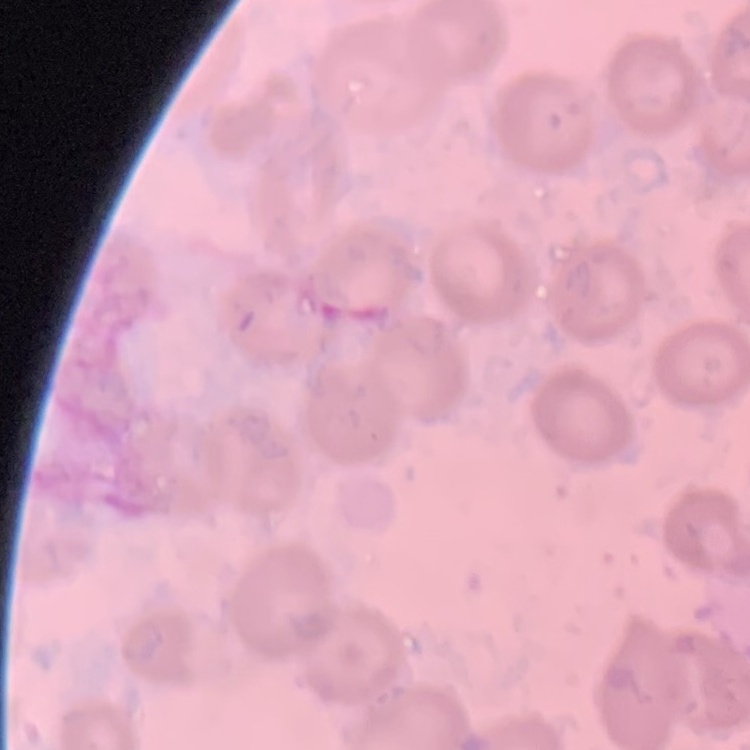

red blood cell morphology = no rouleaux formation
preparation = thin peripheral smear
image type = square crop of a larger photomicrograph
stain = Field's or Giemsa